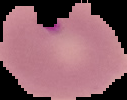

Summary:
  - Result: Plasmodium parasites identified
  - Image size: 127×100 pixels
  - Preparation: thin blood smear
  - Image type: segmented cell region with the area outside set to black